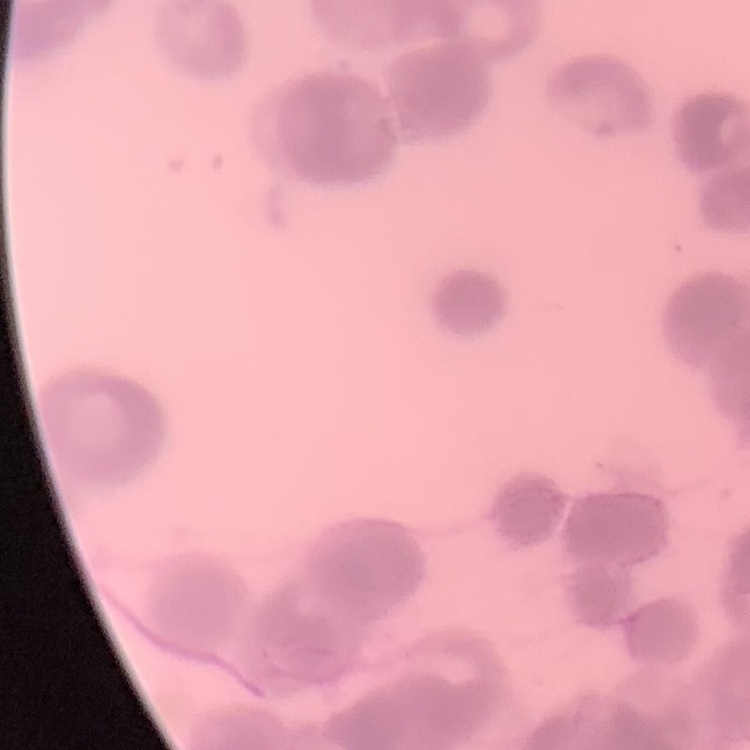

The erythrocytes show rouleaux formation. Field's or Giemsa stain. Square crop of a larger photomicrograph. Thin blood film.